State the preparation type.
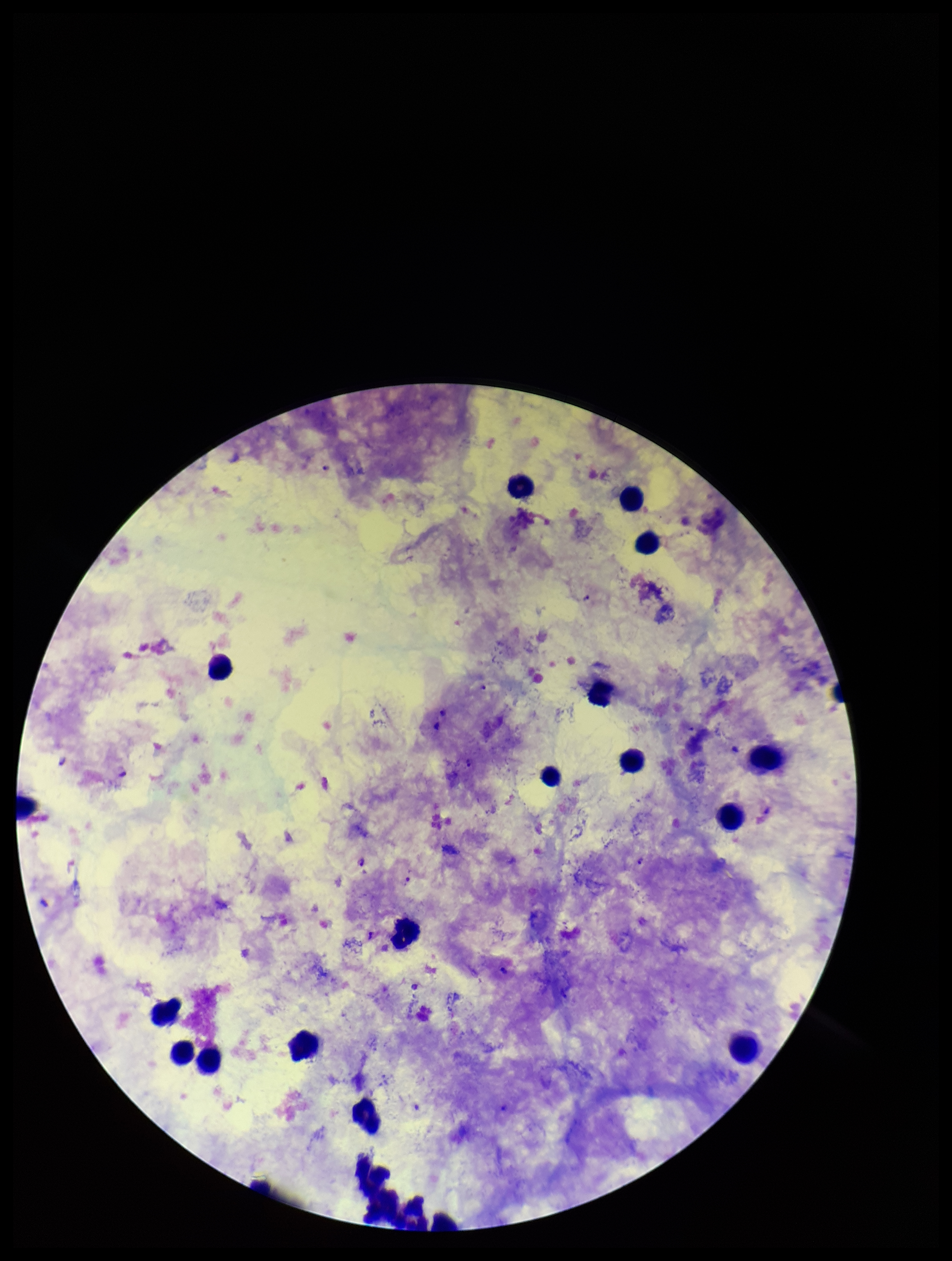
Thick.

Summary:
  - Capture: smartphone photograph through the microscope eyepiece
  - Patient malaria status: positive
  - Plasmodium parasites: detected
  - Species reported for this patient: Plasmodium falciparum
  - Field of view: one from this slide
  - Leukocyte count: 18
  - Stain: Giemsa
  - Parasite count: 4
  - Image size: 952×1261 pixels